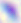

identification: Toxoplasma gondii
modality: photomicrograph
magnification: 400x